State which parasite is depicted.
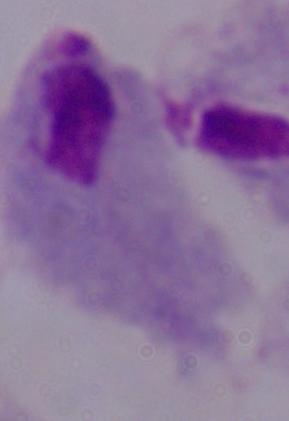

A trichomonad.

modality = micrograph
magnification = 1000x